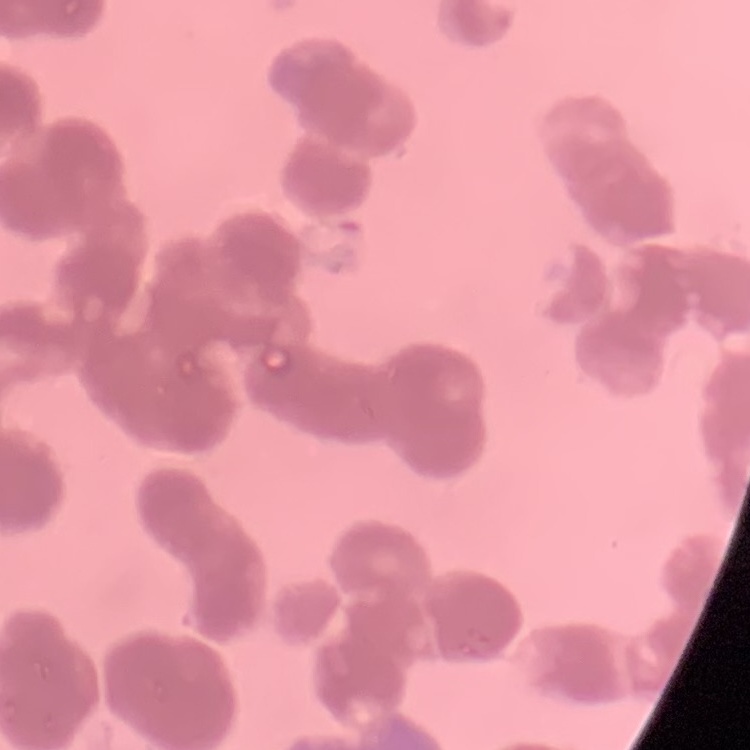
The erythrocytes show rouleaux formation. Thin blood smear. Stained with either Field's or Giemsa. Square crop of a larger photomicrograph.